Assess this cell for malaria.
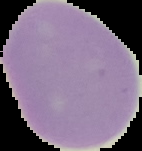

It is uninfected.

image type = segmented cell region with the area outside set to black
image size = 142×151 pixels
preparation = thin blood film